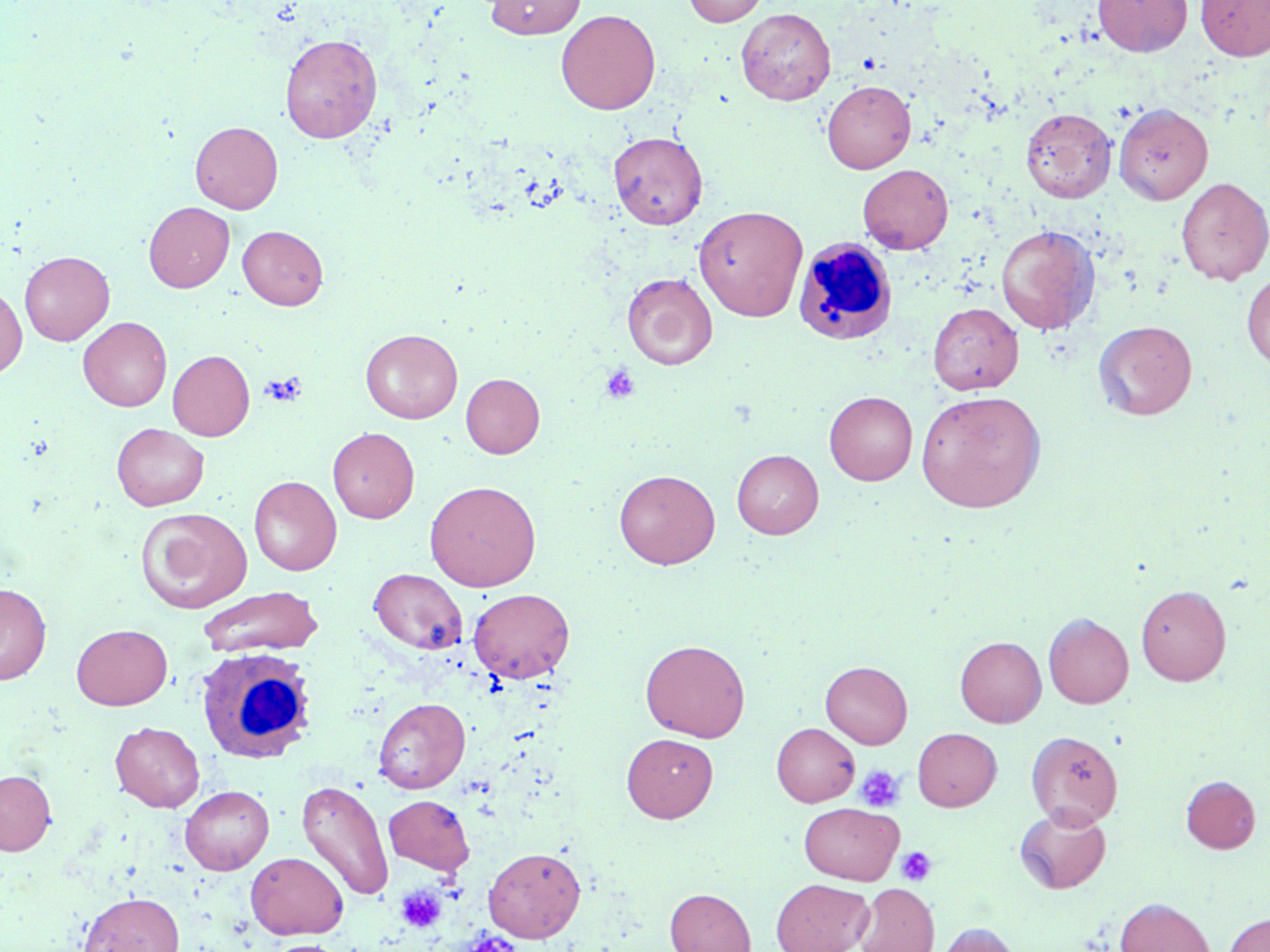
Summary:
  - Coordinate format: approximate bounding boxes as [x1, y1, x2, y2] in pixels
  - Platelet locations: [600, 362, 640, 405], [261, 372, 307, 407], [855, 764, 905, 812], [896, 846, 937, 886], [395, 885, 447, 934]
  - White blood cell locations: [792, 237, 897, 345], [194, 645, 317, 764]
  - Uninfected red blood cell locations: [484, 0, 586, 39], [683, 0, 768, 27], [1093, 0, 1192, 57], [1196, 0, 1270, 61], [736, 8, 835, 105], [556, 9, 660, 115], [280, 33, 382, 143], [822, 80, 916, 173], [1114, 102, 1213, 204], [1020, 107, 1116, 202], [190, 121, 283, 213], [608, 131, 708, 230], [857, 164, 953, 254], [1177, 177, 1270, 285], [144, 201, 235, 293], [693, 205, 808, 321], [996, 224, 1100, 335], [238, 225, 328, 310], [19, 250, 114, 345], [1242, 270, 1270, 371], [622, 272, 717, 371], [0, 284, 27, 379], [928, 303, 1023, 393], [78, 317, 172, 411], [1093, 319, 1197, 420], [361, 329, 462, 423], [168, 350, 255, 440], [461, 373, 545, 458], [916, 390, 1046, 513], [824, 391, 917, 485], [112, 423, 209, 510], [328, 427, 419, 523], [732, 449, 823, 539], [614, 469, 720, 569], [249, 476, 342, 575], [424, 480, 541, 591], [135, 507, 252, 612], [369, 568, 467, 654], [0, 583, 51, 684], [1136, 584, 1231, 686], [197, 586, 324, 658], [468, 588, 574, 683], [1044, 613, 1133, 708], [71, 623, 172, 709], [955, 637, 1046, 727], [641, 639, 750, 741], [820, 661, 912, 748], [372, 697, 470, 794], [110, 721, 205, 811], [772, 723, 859, 807], [913, 728, 1001, 810], [1026, 730, 1123, 828], [622, 733, 718, 822], [0, 769, 56, 855], [1181, 775, 1260, 853], [296, 779, 394, 901], [180, 785, 274, 874], [384, 795, 475, 875], [800, 802, 903, 884], [1014, 805, 1111, 894], [484, 847, 585, 942], [245, 851, 348, 939], [771, 878, 873, 952], [854, 883, 938, 952], [665, 888, 756, 952], [79, 892, 184, 952], [1115, 897, 1215, 952], [1224, 913, 1270, 952], [934, 922, 1021, 952], [265, 939, 347, 952]
  - Slide-level diagnosis: negative for blood parasites
  - Modality: optical microscopy
  - Field of view: one of a larger specimen
  - Preparation: thin blood film
  - Magnification: 1000x
  - Stain: May-Grünwald-Giemsa
  - Image size: 1270×952 pixels